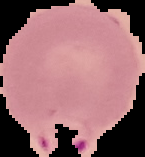

Summary:
  - Image size: 145×157 pixels
  - Preparation: thin blood smear
  - Result: malaria parasites detected
  - Image type: segmented cell region with the area outside set to black